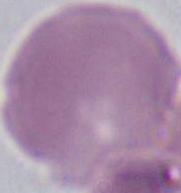
{
  "magnification": "1000x",
  "modality": "micrograph",
  "identification": "erythrocyte"
}